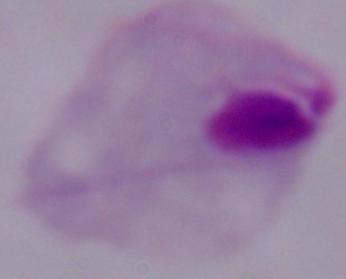
Summary:
  - Magnification: 1000x
  - Modality: micrograph
  - Identification: trichomonad